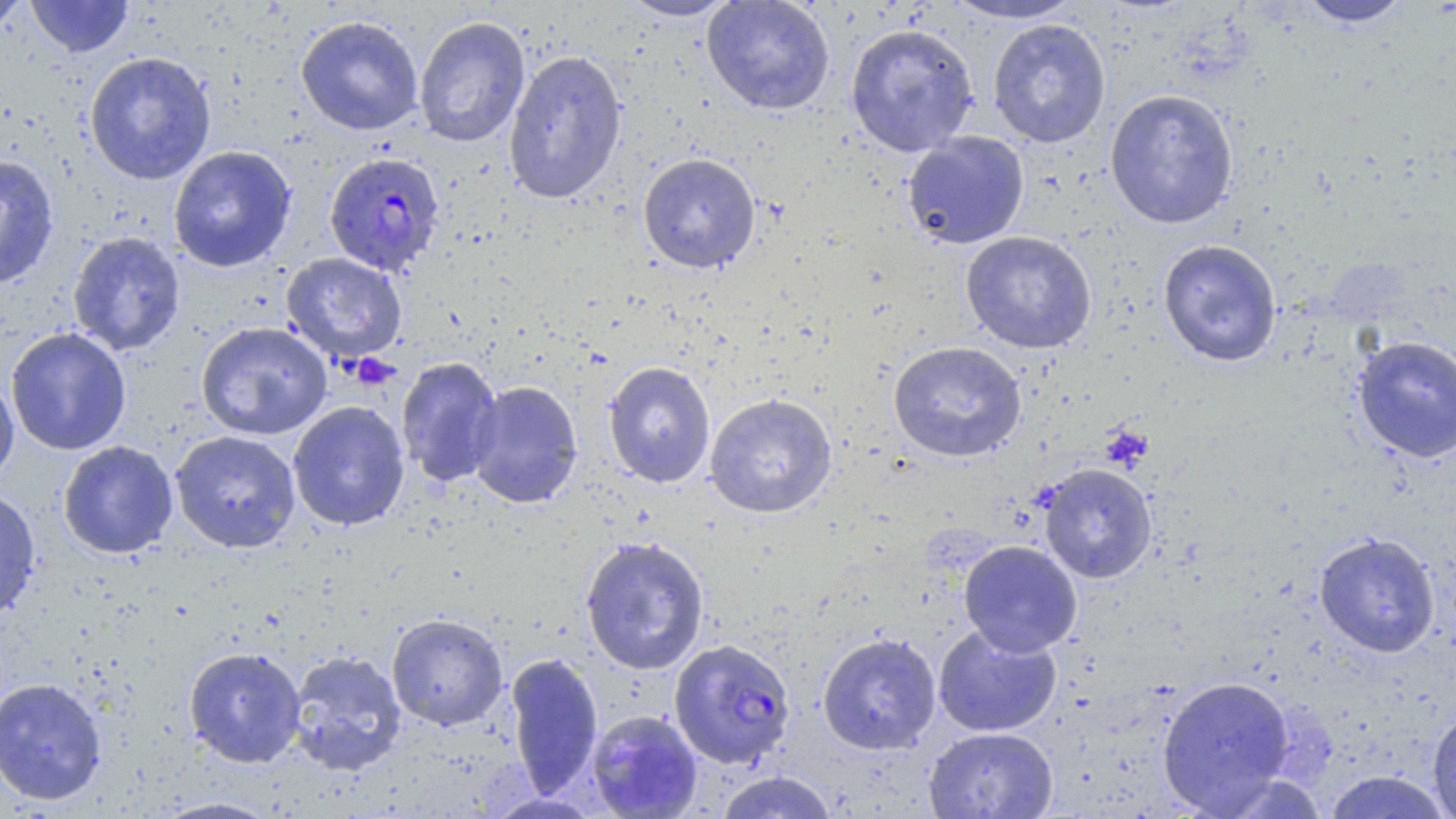
slide_level_diagnosis: Plasmodium falciparum
uninfected_red_blood_cell_locations: 'approximate bounding boxes as named x1/y1/x2/y2 corners in pixels: (x1=26, y1=0, x2=134, y2=58), (x1=616, y1=0, x2=741, y2=21), (x1=701, y1=0, x2=836, y2=115), (x1=939, y1=0, x2=1088, y2=24), (x1=1295, y1=0, x2=1416, y2=28), (x1=0, y1=1, x2=31, y2=37), (x1=295, y1=14, x2=424, y2=135), (x1=413, y1=15, x2=531, y2=148), (x1=987, y1=18, x2=1111, y2=148), (x1=845, y1=23, x2=979, y2=157), (x1=503, y1=49, x2=627, y2=205), (x1=84, y1=51, x2=217, y2=185), (x1=1104, y1=88, x2=1239, y2=229), (x1=902, y1=131, x2=1030, y2=250), (x1=168, y1=145, x2=297, y2=273), (x1=637, y1=153, x2=761, y2=274), (x1=0, y1=155, x2=60, y2=290), (x1=67, y1=231, x2=185, y2=356), (x1=960, y1=231, x2=1097, y2=354), (x1=1158, y1=238, x2=1282, y2=367), (x1=281, y1=252, x2=407, y2=363), (x1=195, y1=321, x2=333, y2=441), (x1=5, y1=328, x2=132, y2=456), (x1=1352, y1=334, x2=1456, y2=463), (x1=888, y1=341, x2=1026, y2=462), (x1=395, y1=356, x2=504, y2=488), (x1=603, y1=361, x2=716, y2=488), (x1=0, y1=371, x2=20, y2=489), (x1=466, y1=380, x2=583, y2=508), (x1=704, y1=393, x2=838, y2=519), (x1=288, y1=401, x2=410, y2=531), (x1=170, y1=430, x2=301, y2=553), (x1=57, y1=441, x2=179, y2=559), (x1=1039, y1=463, x2=1157, y2=583), (x1=0, y1=486, x2=41, y2=622), (x1=1313, y1=531, x2=1441, y2=658), (x1=579, y1=535, x2=710, y2=675), (x1=959, y1=540, x2=1082, y2=657), (x1=386, y1=612, x2=508, y2=731), (x1=933, y1=624, x2=1063, y2=737), (x1=817, y1=632, x2=942, y2=755), (x1=183, y1=647, x2=306, y2=769), (x1=286, y1=649, x2=407, y2=777), (x1=504, y1=652, x2=604, y2=797), (x1=1156, y1=675, x2=1295, y2=814), (x1=0, y1=676, x2=108, y2=806), (x1=585, y1=709, x2=704, y2=818), (x1=1426, y1=709, x2=1456, y2=818), (x1=923, y1=726, x2=1058, y2=818), (x1=713, y1=770, x2=839, y2=818), (x1=1322, y1=770, x2=1453, y2=818), (x1=152, y1=796, x2=283, y2=818)'
stain: May-Grünwald-Giemsa
plasmodium_falciparum_infected_red_blood_cell_locations: 'approximate bounding boxes as named x1/y1/x2/y2 corners in pixels: (x1=324, y1=151, x2=445, y2=276), (x1=669, y1=638, x2=796, y2=769)'
modality: optical microscopy
image_size: 1456×819 pixels
magnification: 1000x
preparation: thin blood film
platelet_locations: 'approximate bounding boxes as named x1/y1/x2/y2 corners in pixels: (x1=348, y1=353, x2=399, y2=390)'
field_of_view: one of a larger specimen